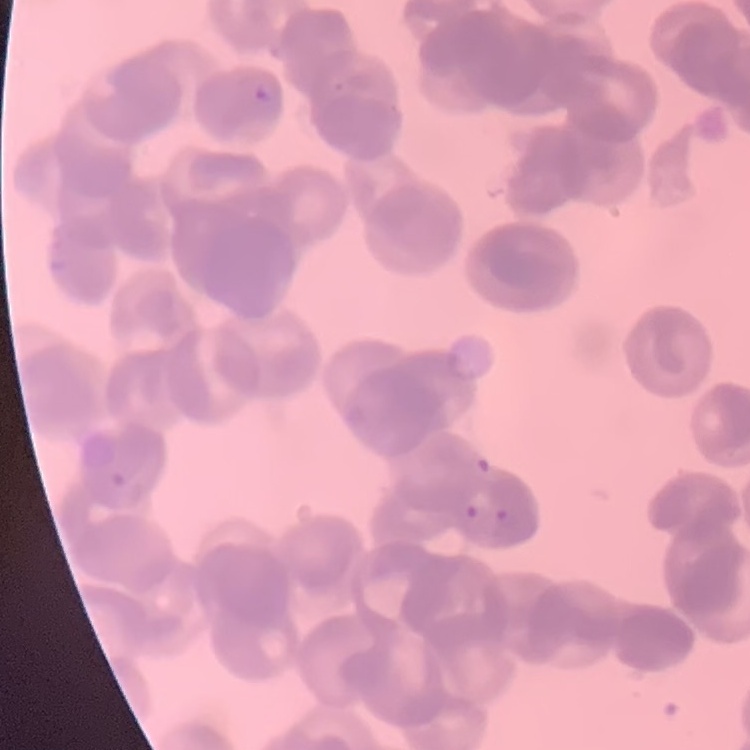 The erythrocytes exhibit rouleaux formation. One tile cut from a larger photomicrograph. Field's or Giemsa stain. Thin peripheral smear.